Classify this cell by malaria status.
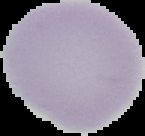

Uninfected.

image type = cell region segmented out of the field of view; surrounding area masked to black
image size = 145×136 pixels
preparation = thin blood smear